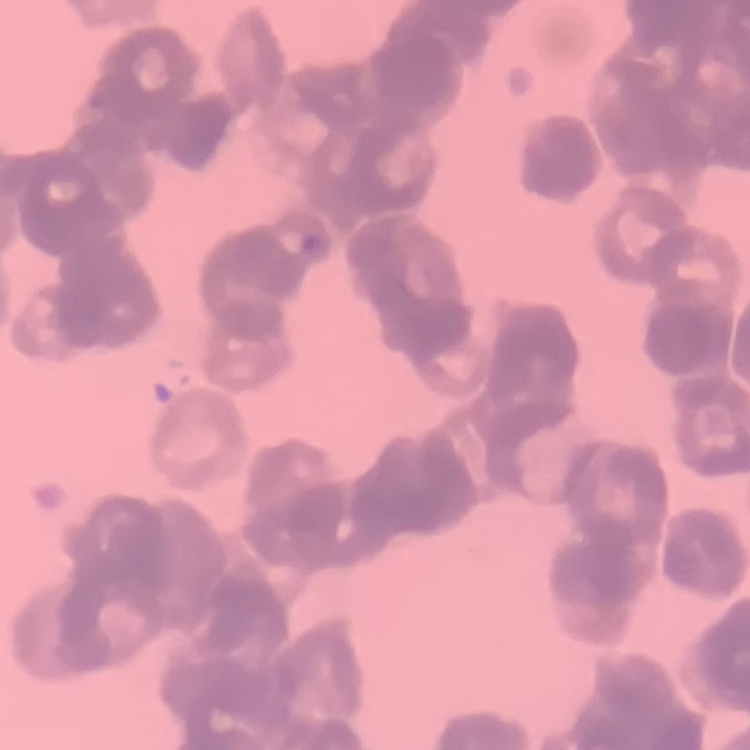
The erythrocytes exhibit rouleaux formation. Field's or Giemsa stain. Thin peripheral smear. Square crop of a larger photomicrograph.